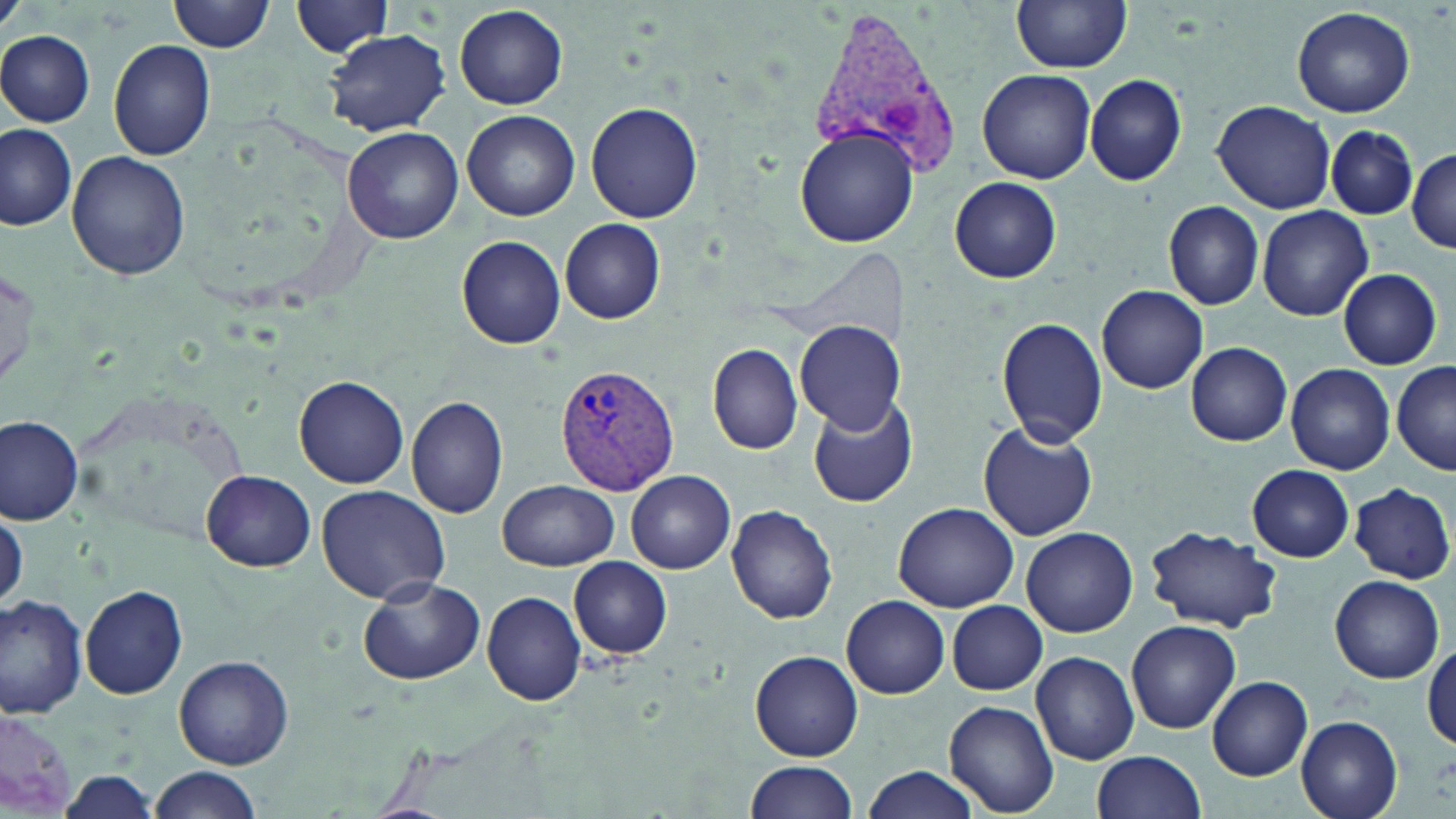 Approximate bounding boxes as [x1, y1, x2, y2] in pixels. Uninfected red blood cell locations: [170, 0, 276, 53], [291, 0, 395, 56], [1012, 0, 1133, 72], [454, 3, 568, 109], [1291, 5, 1415, 119], [325, 30, 449, 136], [0, 31, 95, 126], [108, 40, 216, 160], [977, 68, 1097, 183], [1084, 74, 1189, 185], [1211, 99, 1337, 211], [587, 102, 703, 223], [462, 110, 580, 220], [345, 122, 579, 232], [0, 124, 77, 231], [796, 126, 919, 248], [1327, 126, 1416, 220], [341, 127, 464, 245], [68, 151, 192, 280], [1408, 151, 1456, 251], [950, 176, 1061, 282], [1162, 200, 1265, 310], [1258, 204, 1373, 322], [560, 219, 666, 324], [458, 235, 566, 349], [1337, 269, 1442, 369], [1099, 285, 1207, 393], [997, 316, 1107, 447], [795, 322, 905, 434], [707, 343, 803, 454], [1187, 343, 1291, 447], [1392, 361, 1455, 476], [1285, 363, 1395, 474], [296, 375, 408, 488], [807, 394, 919, 509], [408, 395, 509, 519], [0, 413, 83, 526], [977, 422, 1097, 541], [1247, 464, 1354, 562], [201, 470, 317, 570], [626, 471, 734, 574], [496, 480, 618, 570], [1350, 483, 1453, 582], [318, 485, 451, 605], [893, 502, 1021, 611], [725, 504, 839, 623], [1, 505, 26, 609], [1146, 525, 1279, 633], [1021, 527, 1137, 637], [569, 556, 673, 659], [1329, 574, 1444, 684], [358, 576, 485, 685], [80, 584, 188, 698], [482, 590, 586, 707], [842, 596, 950, 698], [0, 597, 88, 716], [947, 600, 1047, 695], [1126, 619, 1241, 734], [1424, 644, 1456, 753], [750, 649, 864, 761], [1030, 651, 1139, 765], [173, 653, 293, 770], [1207, 676, 1313, 780], [944, 701, 1060, 815], [0, 706, 80, 815], [1296, 715, 1403, 819], [1092, 751, 1208, 818], [745, 760, 858, 819], [147, 766, 263, 819], [863, 766, 978, 819], [56, 773, 160, 816]. Plasmodium vivax-infected red blood cell locations: [808, 7, 966, 182], [553, 363, 680, 497]. Slide-level diagnosis: Plasmodium vivax. 1000x magnification. May-Grünwald-Giemsa stain. Image is 1456×819 pixels. Thin blood film. Optical microscopy. Single field of view.